Classify this cell by malaria status.
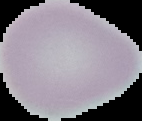

Uninfected.

Image is 142×121 pixels. From a thin blood smear. Cell region segmented out of the field of view; the surrounding area is masked to black.